Report the malaria status of this cell.
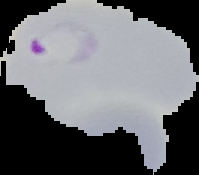

It is parasitized.

preparation = thin blood film
image type = segmented cell region with the area outside set to black
image size = 199×175 pixels